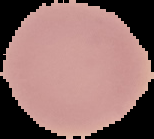
Summary:
  - Preparation: thin blood smear
  - Image size: 154×139 pixels
  - Malaria status: uninfected
  - Image type: segmented cell region with the area outside set to black